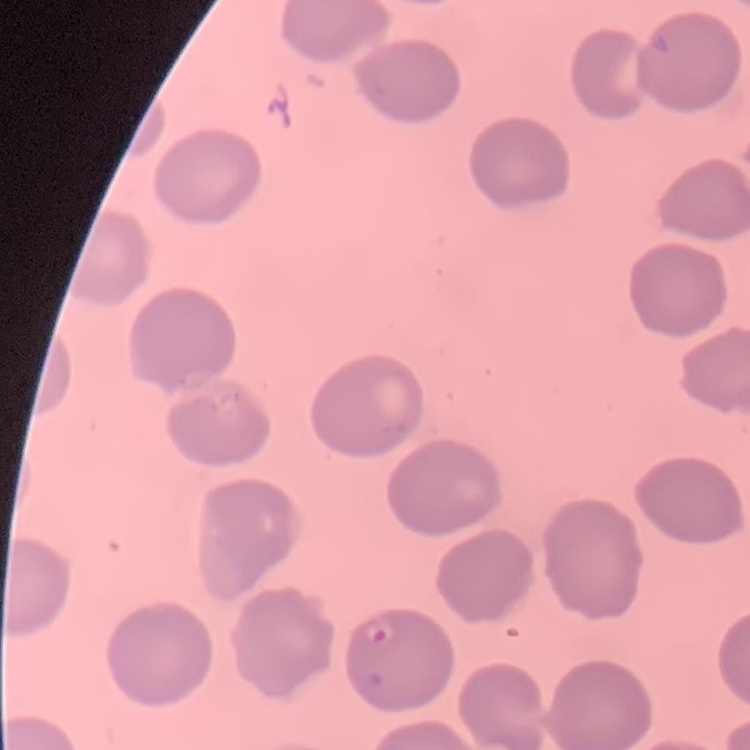
The erythrocytes exhibit no rouleaux formation. Thin blood smear. One tile cut from a larger photomicrograph. Stained with either Field's or Giemsa.